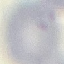

result: no malaria parasites detected
image_type: cell patch, automatically extracted from a larger field of view and resized to 64 × 64 pixels
capture: smartphone camera at the microscope eyepiece
stain: Giemsa
preparation: thin blood film